Give the extent of all Plasmodium falciparum-infected red blood cells.
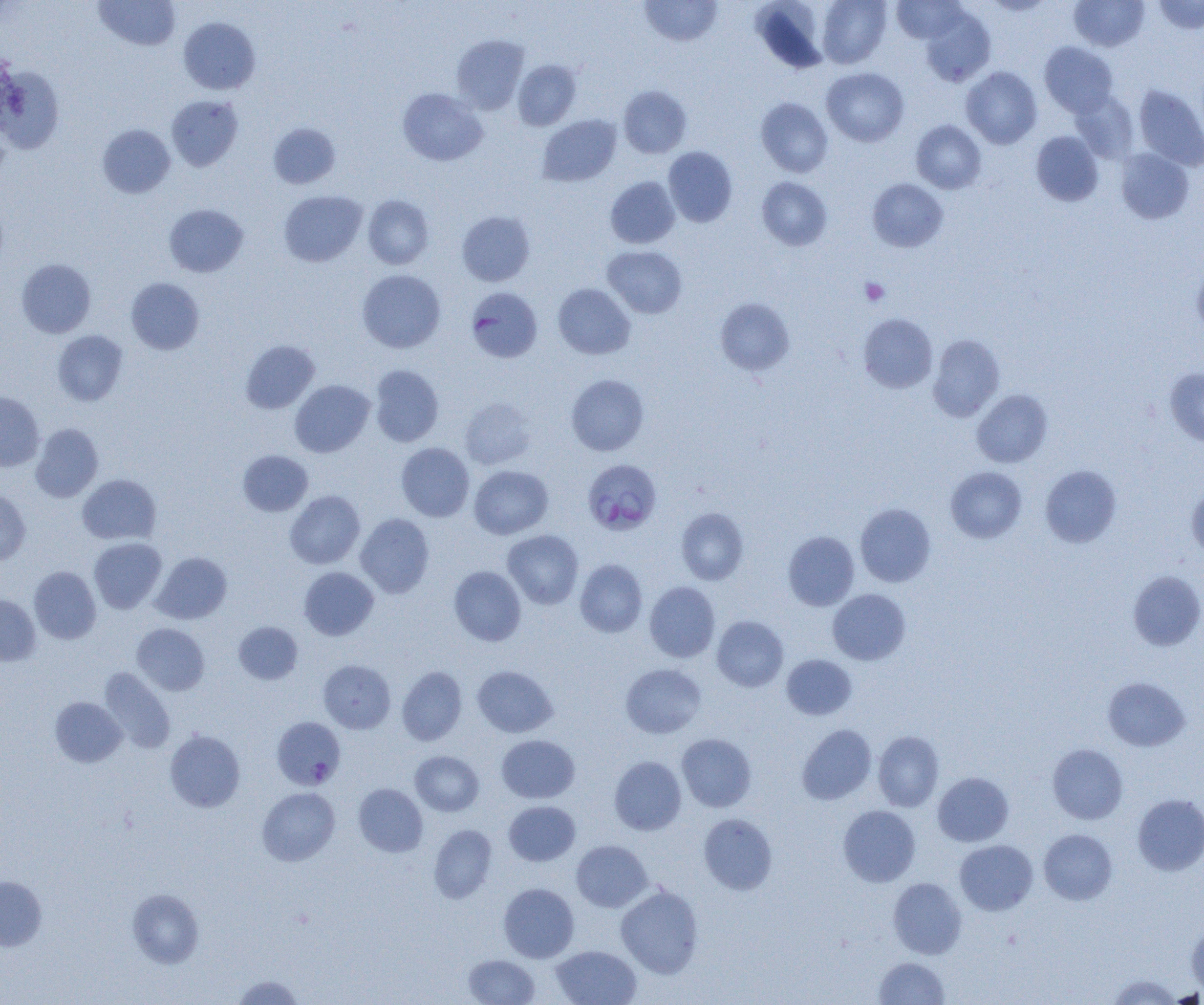

Approximate bounding boxes as [x1, y1, x2, y2] in pixels.
Plasmodium falciparum-infected red blood cells (subset): [583, 459, 662, 535].

Uninfected red blood cell locations (subset): [93, 0, 181, 51], [639, 0, 723, 46], [750, 0, 830, 74], [817, 0, 891, 68], [892, 0, 967, 44], [984, 0, 1055, 16], [1070, 0, 1149, 51], [1154, 0, 1204, 34], [919, 7, 995, 87], [179, 17, 261, 95], [452, 34, 528, 114], [1040, 42, 1118, 117], [513, 60, 581, 130], [0, 66, 65, 152], [961, 66, 1042, 149], [821, 67, 909, 146], [618, 85, 691, 158], [1135, 85, 1204, 170], [397, 88, 487, 166], [1070, 91, 1139, 163], [166, 95, 243, 171], [756, 97, 833, 177], [538, 114, 621, 187], [911, 120, 986, 194], [268, 122, 341, 189], [97, 124, 175, 198], [1031, 131, 1103, 206], [663, 146, 738, 227], [1116, 149, 1194, 224], [605, 176, 680, 248], [757, 177, 832, 250], [867, 178, 948, 252], [279, 189, 367, 267], [363, 195, 433, 269], [164, 203, 248, 277], [457, 211, 535, 286], [603, 245, 687, 318], [17, 258, 96, 338], [1192, 262, 1204, 336], [357, 269, 445, 353], [126, 277, 204, 355], [553, 284, 635, 359], [466, 287, 543, 363], [715, 298, 794, 375], [858, 313, 937, 393], [52, 330, 128, 406], [928, 334, 1005, 421], [241, 339, 320, 414], [369, 365, 444, 446], [1165, 368, 1204, 447], [566, 374, 649, 455], [290, 380, 374, 457], [972, 389, 1052, 467], [0, 392, 44, 471], [460, 397, 536, 469], [31, 423, 103, 502], [396, 442, 474, 521], [238, 450, 313, 516], [469, 465, 553, 539], [1040, 465, 1121, 547], [945, 466, 1026, 543], [77, 474, 161, 544], [1186, 482, 1204, 559], [0, 490, 31, 565], [285, 490, 365, 569], [855, 503, 936, 587], [676, 507, 749, 585], [355, 514, 434, 598], [502, 530, 584, 609], [783, 531, 859, 611], [89, 538, 167, 613], [151, 552, 232, 624], [575, 559, 647, 637], [29, 566, 101, 644], [299, 566, 379, 640], [449, 566, 526, 646], [1129, 571, 1204, 650], [645, 582, 720, 662], [828, 589, 911, 664], [0, 595, 41, 665], [712, 615, 788, 692], [233, 621, 303, 685], [132, 623, 209, 695], [781, 654, 857, 720], [318, 659, 396, 733], [621, 664, 706, 738], [472, 665, 557, 737], [397, 666, 467, 745], [99, 667, 176, 754], [1102, 677, 1190, 751], [50, 697, 126, 767], [797, 724, 876, 805], [165, 729, 245, 812], [873, 730, 944, 811], [677, 733, 756, 811], [497, 735, 579, 803], [1047, 744, 1128, 824], [410, 751, 484, 816], [609, 756, 686, 835], [933, 772, 1013, 846], [354, 783, 428, 857], [257, 787, 340, 866], [1132, 793, 1204, 876], [504, 800, 580, 866], [838, 805, 920, 887], [699, 813, 777, 895], [428, 824, 497, 903], [1039, 829, 1117, 905], [571, 840, 652, 912], [954, 840, 1038, 915], [0, 876, 47, 950], [888, 877, 966, 959], [498, 882, 579, 962], [616, 884, 704, 978], [127, 889, 204, 968], [1186, 925, 1204, 995], [551, 945, 642, 1005], [463, 954, 540, 1004], [874, 956, 950, 1004], [1107, 974, 1184, 1005], [232, 975, 303, 1004]. Platelet locations: [860, 278, 889, 305]. Slide-level diagnosis: Plasmodium falciparum. One field of a larger specimen. Image is 1204×1005 pixels. 1000x magnification. Thin blood film. Optical microscopy.